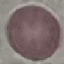
Summary:
  - Malaria status: uninfected
  - Preparation: thin blood film
  - Stain: Giemsa
  - Capture: smartphone through the microscope eyepiece
  - Image type: automatically extracted cell patch, resized to 64 × 64 pixels